Classify this cell by malaria status.
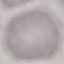
Uninfected.

stain: Giemsa
preparation: thin blood film
image_type: automatically extracted cell patch, resized to 64 × 64 pixels
capture: smartphone through the microscope eyepiece